Assess the morphology of the red blood cells.
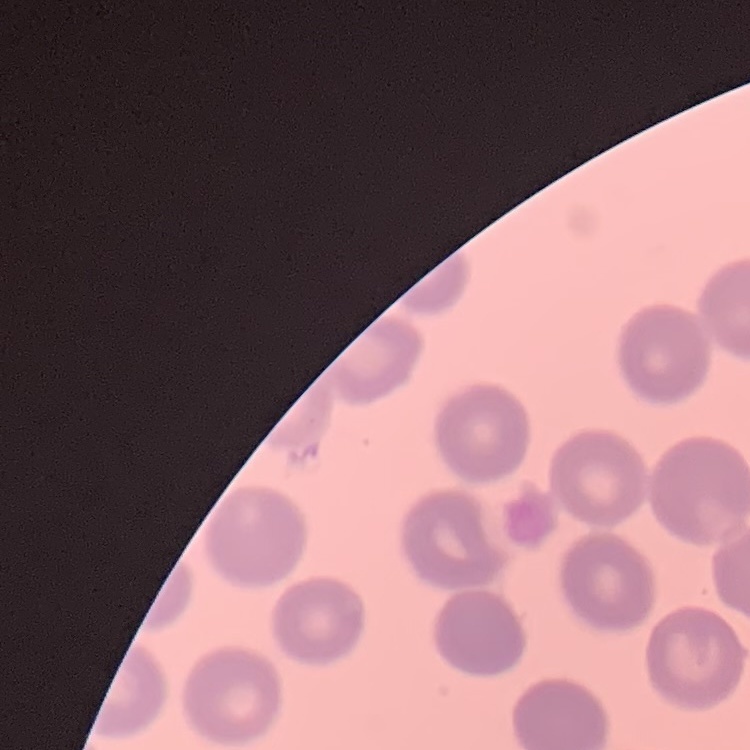

No rouleaux formation.

Summary:
  - Image type: one tile cut from a larger photomicrograph
  - Preparation: thin blood film
  - Stain: Field's or Giemsa